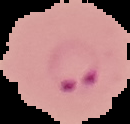
Summary:
  - Result: malaria parasites detected
  - Image size: 130×124 pixels
  - Image type: cell region segmented out of the field of view; surrounding area masked to black
  - Preparation: thin blood smear